Assess for Plasmodium parasites.
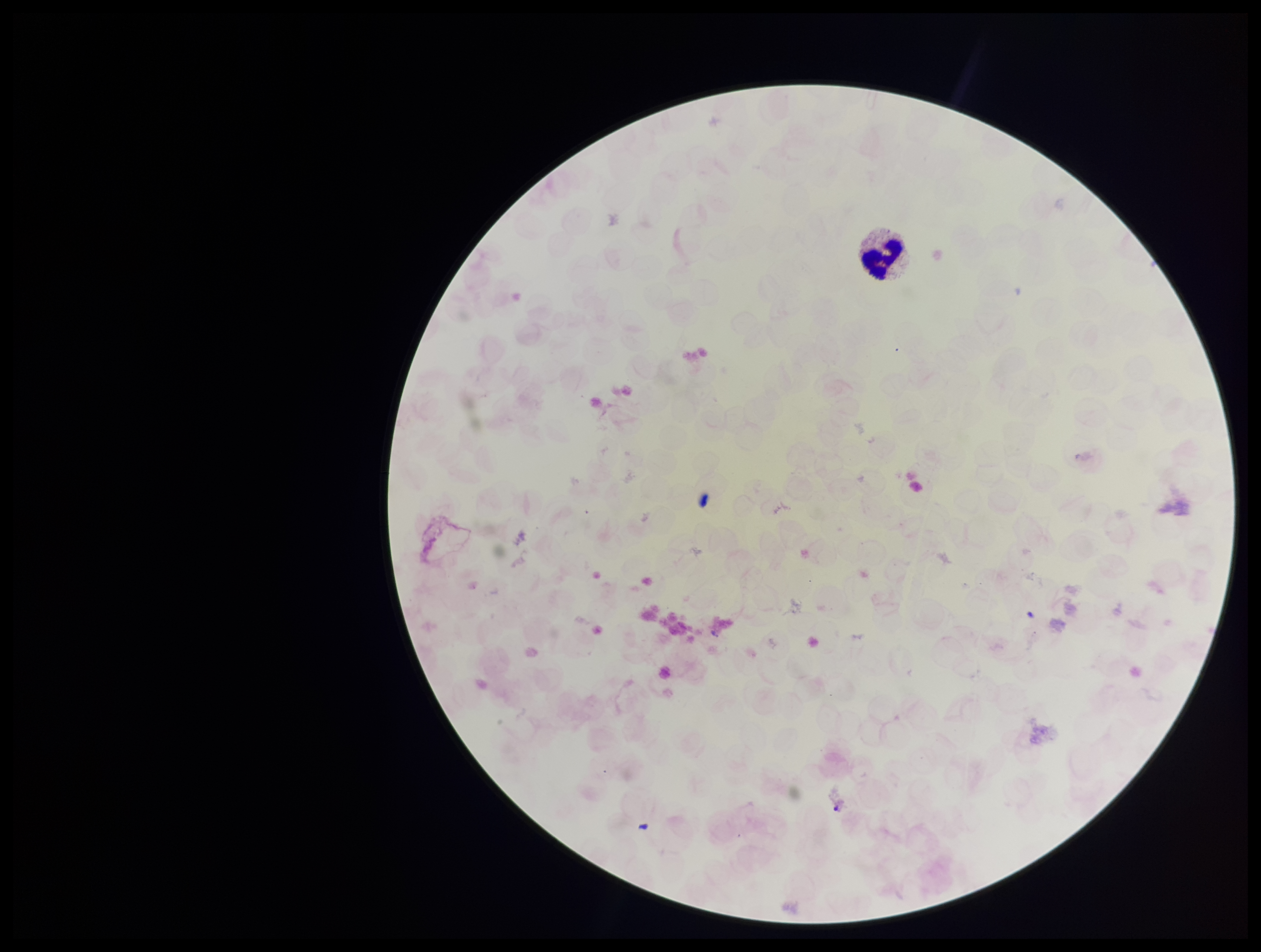

Identified.

Summary:
  - Stain: Giemsa
  - Capture: smartphone photograph through the microscope eyepiece
  - Image size: 1261×952 pixels
  - Leukocyte count: 1
  - Parasite count: 1
  - Patient malaria status: positive
  - Preparation: thick
  - Field of view: single
  - Species reported for this patient: Plasmodium vivax